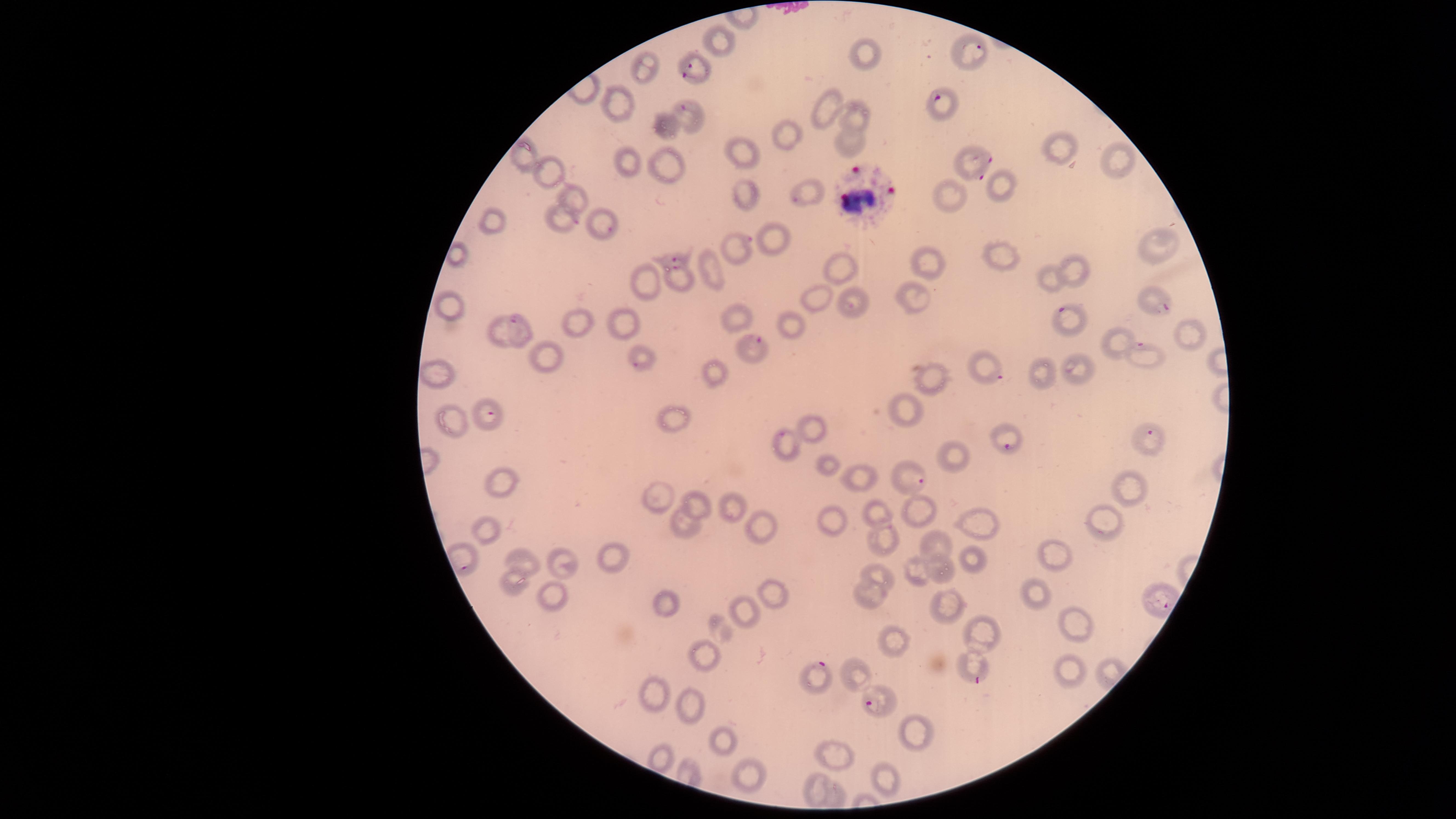

field of view = single
capture = smartphone photograph through the microscope eyepiece
parasitized red blood cells = approximate marker points as (x, y) in pixels: (976, 47), (695, 67), (937, 97), (689, 108), (979, 163), (796, 199), (567, 217), (608, 227), (741, 244), (673, 258), (676, 269), (1162, 301), (851, 305), (1074, 322), (516, 324), (751, 346), (1150, 355), (638, 366), (990, 369), (490, 411), (1148, 433), (783, 436), (1008, 445), (921, 482), (817, 666), (975, 682), (867, 704)
presence = malaria parasites identified
stain = Giemsa
white blood cells = approximate marker points as (x, y) in pixels: (861, 188)
species = Plasmodium falciparum
uninfected red blood cells = approximate marker points as (x, y) in pixels: (723, 40), (867, 59), (641, 71), (835, 94), (615, 105), (857, 119), (670, 127), (790, 136), (854, 140), (1062, 145), (526, 151), (751, 154), (1123, 161), (667, 162), (628, 164), (555, 168), (1005, 187), (746, 189), (578, 194), (946, 197), (495, 226), (778, 235), (1157, 247), (1003, 259), (928, 260), (844, 267), (1071, 268), (713, 275), (1051, 278), (647, 279), (918, 297), (822, 298), (450, 305), (735, 319), (624, 321), (794, 323), (575, 325), (1179, 335), (1116, 341), (548, 357), (444, 370), (1046, 371), (1082, 371), (715, 373), (935, 378), (907, 404), (680, 420), (449, 423), (819, 426), (957, 458), (828, 463), (857, 476), (499, 481), (1129, 487), (659, 496), (700, 504), (727, 508), (920, 511), (881, 513), (835, 519), (1111, 524), (685, 526), (765, 526), (980, 526), (479, 529), (891, 539), (935, 541), (1060, 552), (971, 558), (524, 562), (610, 562), (557, 564), (920, 570), (946, 572), (880, 574), (516, 588), (870, 593), (558, 594), (774, 596), (1038, 596), (669, 604), (948, 604), (748, 611), (1074, 627), (983, 630), (897, 641), (707, 654), (1070, 671), (862, 678), (652, 689), (693, 702), (917, 728), (722, 737), (663, 758), (839, 758), (753, 781), (815, 781), (887, 781)
visible region = circular
image size = 1456×819 pixels
preparation = thin blood smear